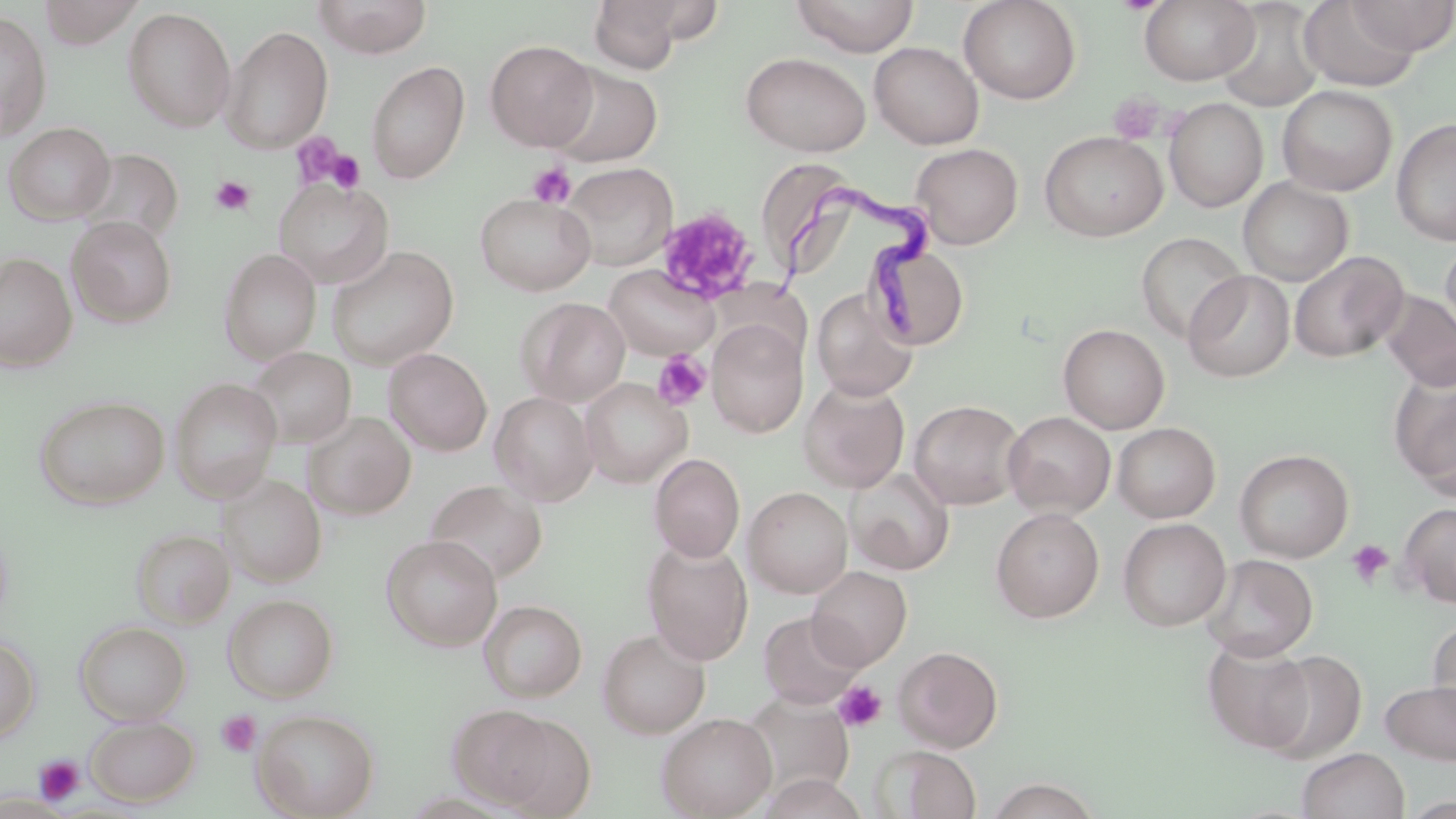
Approximate bounding boxes as [x1, y1, x2, y2] in pixels. Uninfected red blood cell locations (subset): [35, 0, 147, 49], [313, 0, 431, 58], [588, 0, 689, 74], [791, 0, 919, 57], [958, 0, 1081, 105], [1139, 0, 1259, 86], [1298, 0, 1420, 91], [1343, 0, 1456, 55], [1215, 1, 1325, 112], [123, 6, 236, 133], [0, 10, 52, 141], [221, 25, 333, 154], [485, 40, 598, 151], [869, 42, 983, 149], [740, 51, 871, 157], [366, 61, 470, 184], [546, 64, 662, 167], [1277, 85, 1397, 196], [1164, 97, 1268, 213], [1391, 118, 1456, 246], [3, 122, 115, 225], [1040, 131, 1167, 242], [911, 143, 1023, 249], [75, 148, 183, 244], [756, 157, 856, 286], [559, 162, 677, 271], [1238, 177, 1353, 287], [272, 178, 394, 289], [475, 193, 595, 295], [67, 217, 177, 327], [1137, 232, 1246, 344], [1440, 239, 1456, 347], [867, 243, 968, 351], [326, 245, 459, 370], [219, 248, 321, 364], [1289, 251, 1409, 363], [1, 253, 76, 371], [1183, 270, 1296, 382], [811, 287, 919, 401], [1380, 291, 1456, 392], [516, 297, 630, 406], [707, 319, 807, 437], [1058, 324, 1170, 434], [246, 347, 356, 449], [384, 348, 492, 456], [1391, 370, 1456, 494], [169, 377, 282, 503], [580, 378, 692, 488], [799, 379, 910, 493], [489, 391, 598, 506], [34, 395, 170, 509], [908, 399, 1026, 510], [1003, 411, 1115, 519], [303, 412, 416, 520], [1113, 422, 1221, 523], [1234, 449, 1354, 563], [649, 454, 745, 562], [845, 467, 954, 575], [219, 474, 326, 587], [424, 479, 547, 585], [744, 487, 853, 598], [1398, 503, 1456, 607], [991, 507, 1104, 623], [1118, 518, 1231, 631], [131, 528, 234, 628], [381, 534, 502, 651], [641, 539, 754, 666], [1200, 553, 1318, 662], [807, 565, 911, 670], [223, 594, 338, 702], [480, 600, 587, 702], [758, 611, 865, 709], [1427, 618, 1456, 729], [75, 620, 191, 724], [597, 629, 710, 738], [0, 635, 40, 743], [1203, 638, 1317, 753], [894, 645, 1003, 751], [1260, 650, 1366, 764], [1379, 680, 1456, 764], [737, 693, 854, 802], [447, 704, 561, 809], [252, 709, 379, 819], [656, 712, 777, 818], [85, 715, 199, 806], [488, 715, 597, 816], [876, 745, 982, 819], [1297, 747, 1410, 819], [758, 774, 869, 819], [983, 777, 1104, 819]. Platelet locations (subset): [1108, 92, 1165, 144], [289, 133, 354, 192], [324, 149, 366, 193], [527, 162, 575, 208], [210, 175, 255, 216], [657, 208, 758, 305], [653, 349, 712, 411], [1346, 539, 1394, 588], [833, 679, 888, 732], [217, 711, 261, 757], [34, 755, 86, 806]. Trypanosoma brucei locations: [767, 169, 948, 336]. Slide-level diagnosis: Trypanosoma brucei. Thin blood film. Single field of view. Optical microscopy. May-Grünwald-Giemsa stain. 1000x magnification. Image is 1456×819 pixels.